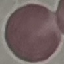

Summary:
  - Malaria status: uninfected
  - Stain: Giemsa
  - Image type: automatically extracted cell patch, resized to 64 × 64 pixels
  - Capture: smartphone camera at the microscope eyepiece
  - Preparation: thin smear